State the preparation type.
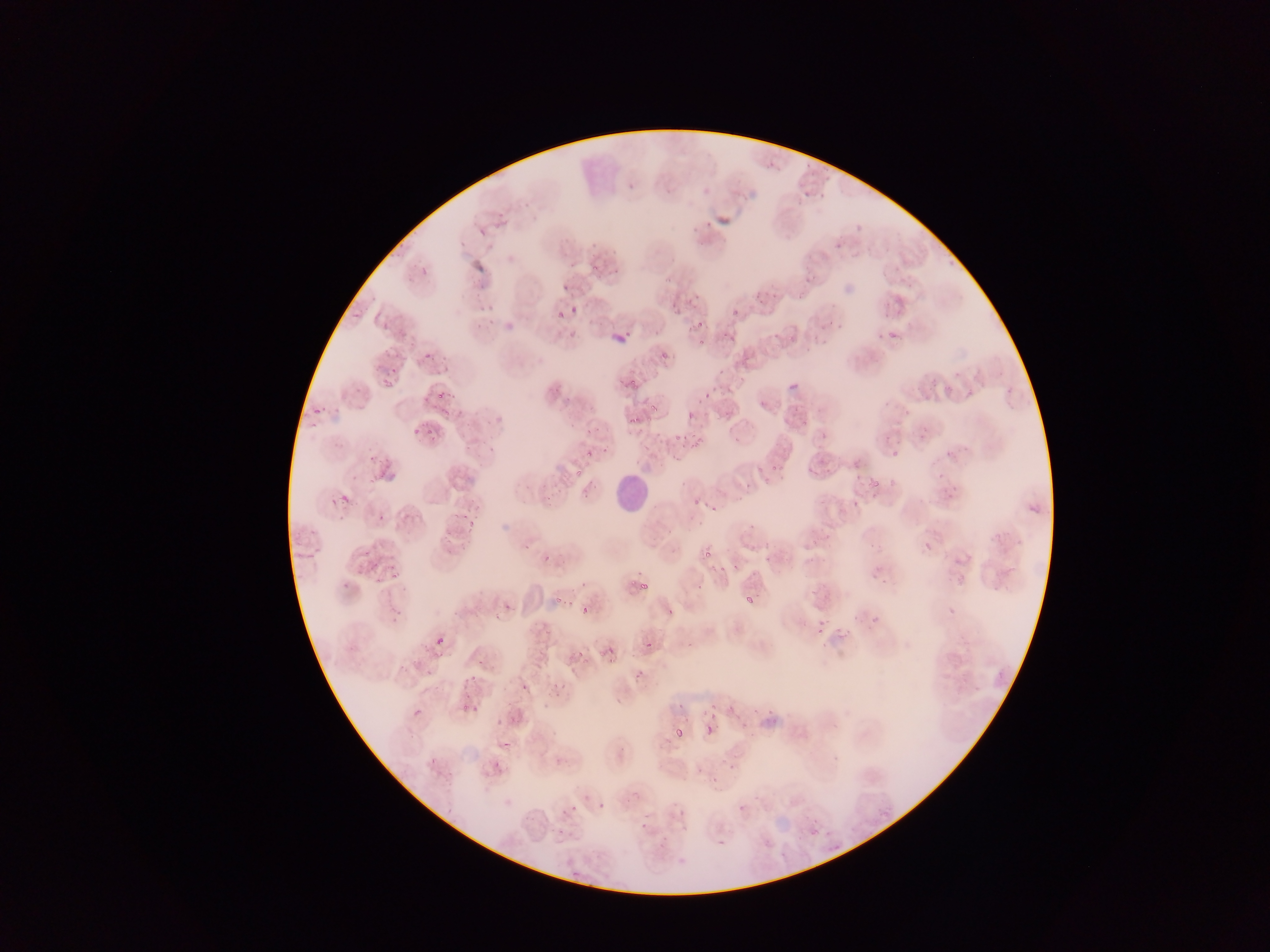
This is a thin smear.

Approximate bounding boxes as (left, top, right, bottom) in pixels. Plasmodium parasite locations: (627, 173, 647, 189), (523, 197, 533, 205), (472, 224, 488, 235), (416, 265, 435, 278), (611, 266, 619, 276), (659, 273, 675, 285), (563, 283, 570, 291), (681, 291, 697, 305), (351, 300, 371, 325), (476, 302, 500, 326), (566, 305, 582, 322), (724, 307, 745, 320), (381, 309, 397, 331), (549, 310, 566, 322), (692, 316, 704, 328), (604, 321, 628, 345), (722, 323, 743, 347), (698, 340, 706, 347), (423, 352, 434, 362), (656, 352, 673, 366), (785, 368, 804, 393), (377, 370, 396, 393), (628, 379, 637, 388), (430, 391, 456, 413), (703, 391, 711, 399), (652, 408, 661, 420), (687, 410, 696, 420), (301, 411, 328, 429), (622, 414, 640, 428), (408, 417, 421, 444), (577, 424, 597, 434), (419, 431, 438, 443), (671, 433, 689, 449), (584, 447, 597, 460), (891, 450, 901, 459), (364, 451, 386, 474), (764, 461, 786, 485), (567, 468, 586, 484), (807, 468, 817, 477), (933, 470, 950, 484), (864, 475, 876, 490), (887, 478, 895, 487), (738, 481, 754, 496), (689, 485, 709, 517), (339, 494, 349, 503), (849, 499, 864, 515), (710, 504, 721, 517), (460, 508, 480, 536), (923, 541, 932, 551), (358, 547, 377, 572), (759, 547, 774, 564), (702, 549, 712, 559), (382, 552, 411, 572), (542, 553, 553, 562), (717, 562, 735, 577), (377, 567, 406, 599), (737, 572, 767, 610), (634, 576, 656, 596), (554, 596, 562, 605), (581, 606, 589, 615), (665, 606, 673, 616), (867, 611, 882, 629), (799, 621, 807, 629), (817, 622, 826, 631), (434, 636, 445, 646), (638, 637, 658, 657), (572, 639, 587, 685), (819, 642, 827, 650), (593, 645, 616, 664), (629, 663, 647, 687), (516, 668, 533, 693), (550, 673, 572, 700), (467, 675, 476, 683), (720, 695, 741, 725), (460, 700, 481, 719), (670, 700, 687, 710), (707, 705, 719, 723), (412, 707, 423, 717), (705, 724, 715, 734), (676, 729, 684, 737), (496, 734, 518, 752), (428, 758, 437, 766), (492, 761, 503, 772), (727, 763, 737, 776), (713, 774, 721, 782), (597, 799, 607, 809), (570, 804, 579, 812), (678, 808, 687, 818), (637, 821, 650, 833), (715, 832, 725, 847). Leukocyte locations: (609, 471, 649, 514). Image is 1270×952 pixels. Collected in Ghana. Mobile-phone photograph taken through the microscope. Single field of view.